Outline each Trypanosoma brucei.
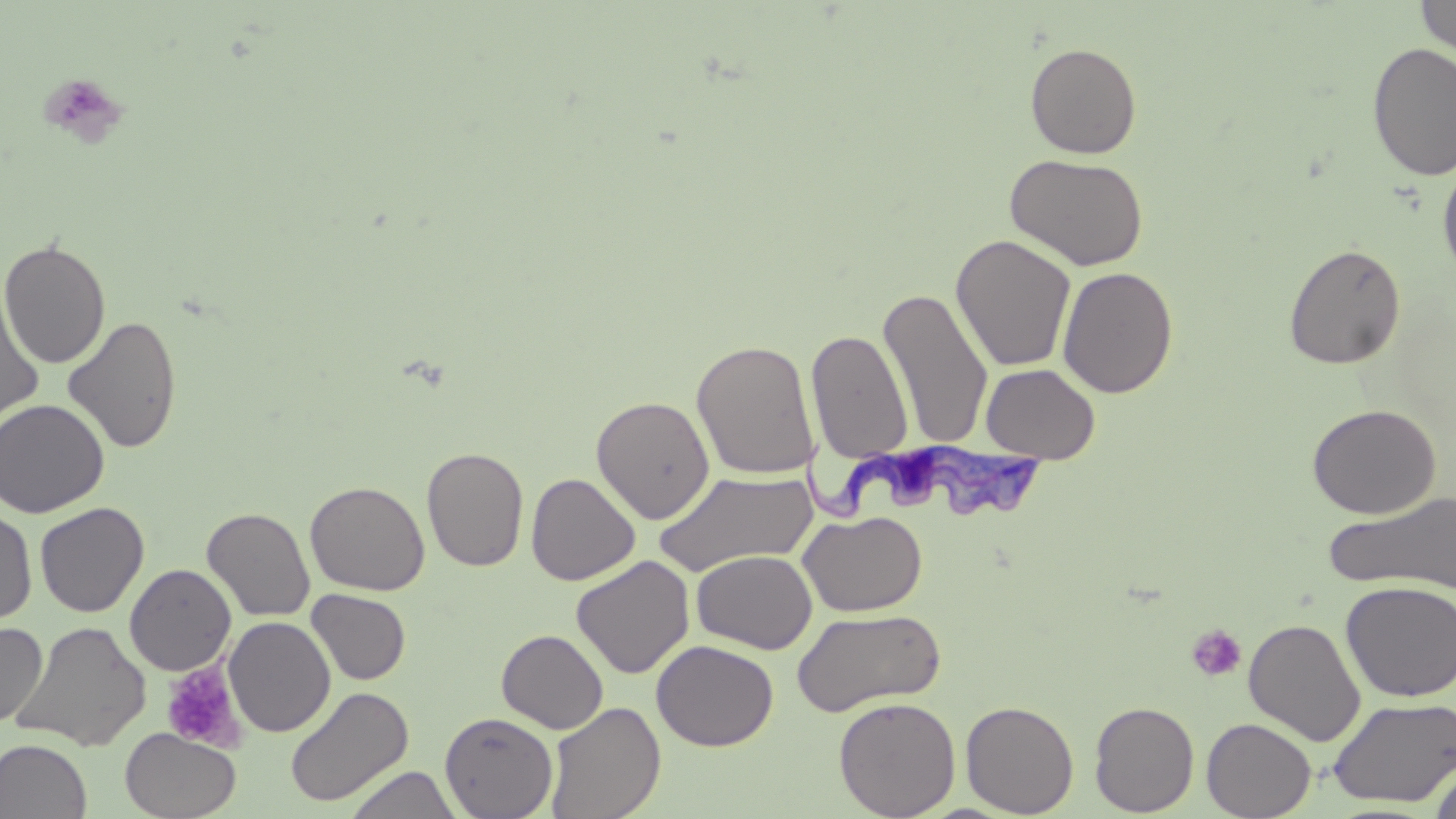

Approximate bounding boxes as named x1/y1/x2/y2 corners in pixels.
Trypanosoma brucei: (x1=800, y1=429, x2=1052, y2=522).

slide-level diagnosis = Trypanosoma brucei
image size = 1456×819 pixels
platelet locations = approximate bounding boxes as named x1/y1/x2/y2 corners in pixels: (x1=36, y1=71, x2=129, y2=149), (x1=1185, y1=624, x2=1248, y2=683), (x1=161, y1=662, x2=244, y2=753)
magnification = 1000x
stain = May-Grünwald-Giemsa
uninfected red blood cell locations = approximate bounding boxes as named x1/y1/x2/y2 corners in pixels: (x1=1416, y1=0, x2=1456, y2=58), (x1=1025, y1=42, x2=1142, y2=159), (x1=1367, y1=43, x2=1456, y2=181), (x1=1004, y1=152, x2=1150, y2=272), (x1=1437, y1=158, x2=1456, y2=286), (x1=951, y1=234, x2=1076, y2=372), (x1=0, y1=238, x2=111, y2=369), (x1=1284, y1=243, x2=1406, y2=370), (x1=1057, y1=266, x2=1179, y2=399), (x1=878, y1=285, x2=994, y2=452), (x1=0, y1=286, x2=45, y2=430), (x1=63, y1=315, x2=182, y2=455), (x1=806, y1=329, x2=914, y2=463), (x1=691, y1=339, x2=819, y2=479), (x1=981, y1=363, x2=1100, y2=464), (x1=591, y1=395, x2=715, y2=524), (x1=0, y1=398, x2=109, y2=518), (x1=1307, y1=403, x2=1441, y2=518), (x1=422, y1=446, x2=528, y2=572), (x1=653, y1=468, x2=819, y2=577), (x1=526, y1=472, x2=640, y2=585), (x1=305, y1=480, x2=430, y2=596), (x1=1322, y1=489, x2=1456, y2=596), (x1=35, y1=502, x2=149, y2=617), (x1=202, y1=506, x2=315, y2=621), (x1=0, y1=508, x2=37, y2=625), (x1=798, y1=510, x2=928, y2=617), (x1=691, y1=549, x2=817, y2=654), (x1=571, y1=555, x2=695, y2=679), (x1=124, y1=563, x2=236, y2=676), (x1=1340, y1=580, x2=1455, y2=703), (x1=306, y1=589, x2=411, y2=685), (x1=791, y1=607, x2=946, y2=717), (x1=224, y1=616, x2=336, y2=737), (x1=1243, y1=618, x2=1366, y2=746), (x1=11, y1=620, x2=152, y2=752), (x1=0, y1=622, x2=47, y2=728), (x1=496, y1=629, x2=608, y2=733), (x1=652, y1=639, x2=778, y2=751), (x1=285, y1=686, x2=413, y2=808), (x1=833, y1=696, x2=961, y2=818), (x1=1328, y1=696, x2=1456, y2=806), (x1=960, y1=699, x2=1079, y2=817), (x1=1089, y1=700, x2=1200, y2=816), (x1=544, y1=701, x2=665, y2=819), (x1=439, y1=711, x2=558, y2=819), (x1=1201, y1=717, x2=1316, y2=819), (x1=121, y1=728, x2=240, y2=818), (x1=0, y1=739, x2=92, y2=819), (x1=1428, y1=760, x2=1456, y2=819), (x1=344, y1=765, x2=462, y2=818)
preparation = thin blood smear
field of view = single
modality = optical microscopy